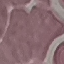
malaria status = uninfected
capture = smartphone camera at the microscope eyepiece
preparation = thin blood film
image type = automatically extracted cell patch, resized to 64 × 64 pixels
stain = Giemsa